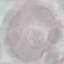
Summary:
  - Malaria status: uninfected
  - Image type: automatically extracted cell patch, resized to 64 × 64 pixels
  - Capture: smartphone camera at the microscope eyepiece
  - Preparation: thin smear
  - Stain: Giemsa